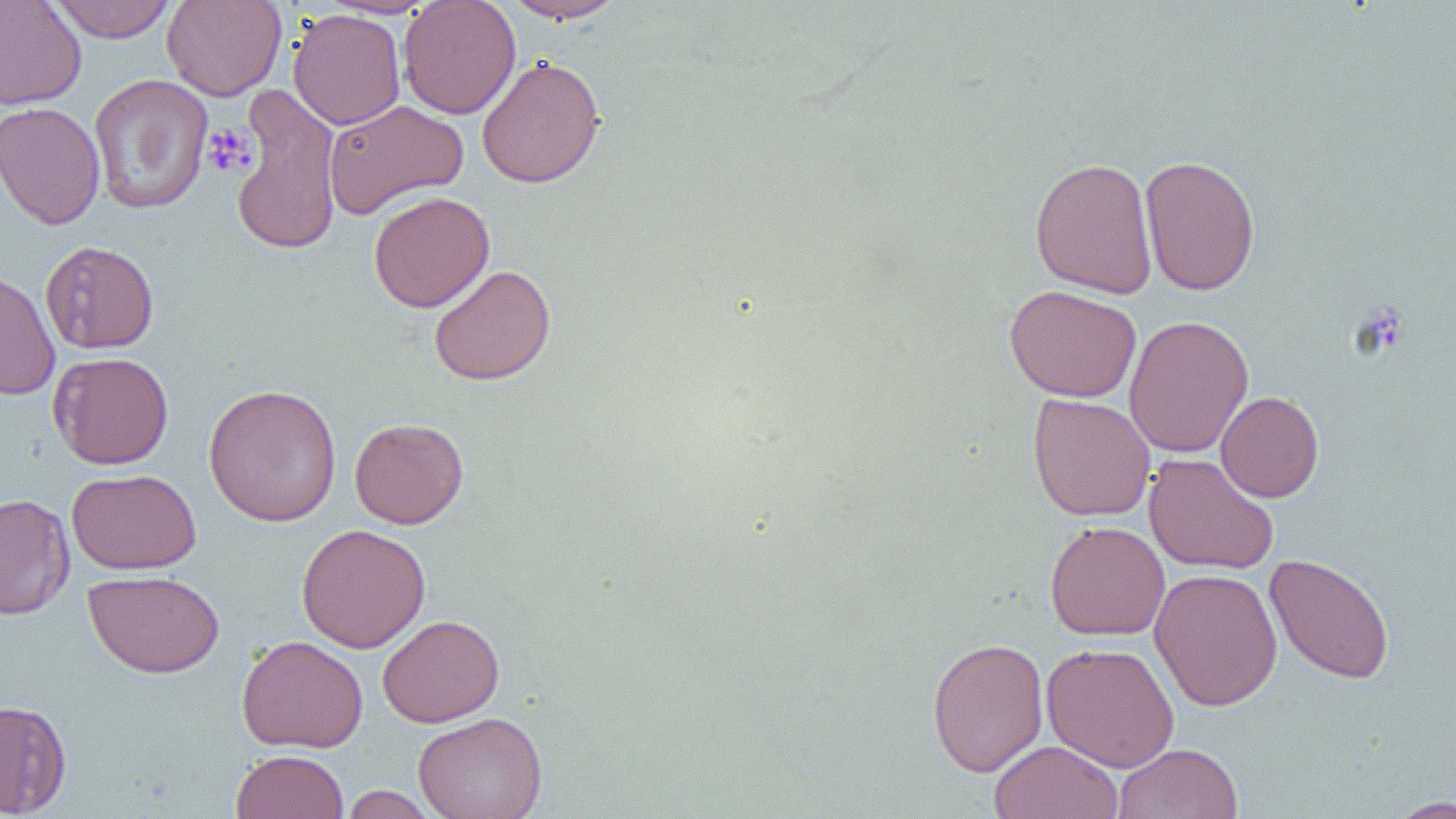
slide-level diagnosis = negative for blood parasites
image size = 1456×819 pixels
field of view = single
modality = optical microscopy
magnification = 1000x
platelet locations = approximate bounding boxes as named x1/y1/x2/y2 corners in pixels: (x1=202, y1=124, x2=257, y2=178)
preparation = thin blood film
uninfected red blood cell locations = approximate bounding boxes as named x1/y1/x2/y2 corners in pixels: (x1=0, y1=0, x2=87, y2=110), (x1=48, y1=0, x2=177, y2=42), (x1=161, y1=0, x2=287, y2=101), (x1=501, y1=0, x2=629, y2=24), (x1=397, y1=1, x2=520, y2=119), (x1=288, y1=9, x2=406, y2=130), (x1=476, y1=55, x2=605, y2=189), (x1=88, y1=74, x2=213, y2=215), (x1=228, y1=84, x2=344, y2=257), (x1=323, y1=99, x2=469, y2=219), (x1=0, y1=101, x2=105, y2=231), (x1=1139, y1=154, x2=1260, y2=296), (x1=1029, y1=156, x2=1158, y2=299), (x1=368, y1=191, x2=495, y2=313), (x1=40, y1=240, x2=159, y2=354), (x1=428, y1=264, x2=556, y2=386), (x1=0, y1=269, x2=61, y2=400), (x1=1004, y1=285, x2=1141, y2=403), (x1=1123, y1=314, x2=1254, y2=459), (x1=48, y1=352, x2=174, y2=469), (x1=202, y1=383, x2=342, y2=527), (x1=1216, y1=391, x2=1324, y2=502), (x1=1028, y1=393, x2=1155, y2=522), (x1=349, y1=417, x2=469, y2=529), (x1=1143, y1=453, x2=1280, y2=575), (x1=66, y1=468, x2=201, y2=574), (x1=0, y1=493, x2=76, y2=621), (x1=1045, y1=520, x2=1170, y2=641), (x1=296, y1=523, x2=430, y2=653), (x1=1264, y1=552, x2=1395, y2=684), (x1=1149, y1=568, x2=1283, y2=711), (x1=83, y1=569, x2=225, y2=678), (x1=377, y1=614, x2=504, y2=727), (x1=236, y1=634, x2=368, y2=753), (x1=926, y1=636, x2=1049, y2=777), (x1=1041, y1=642, x2=1180, y2=772), (x1=0, y1=699, x2=72, y2=816), (x1=413, y1=711, x2=548, y2=819), (x1=988, y1=740, x2=1124, y2=818), (x1=1113, y1=742, x2=1243, y2=819), (x1=230, y1=750, x2=349, y2=819), (x1=341, y1=785, x2=438, y2=818), (x1=1386, y1=796, x2=1456, y2=818)